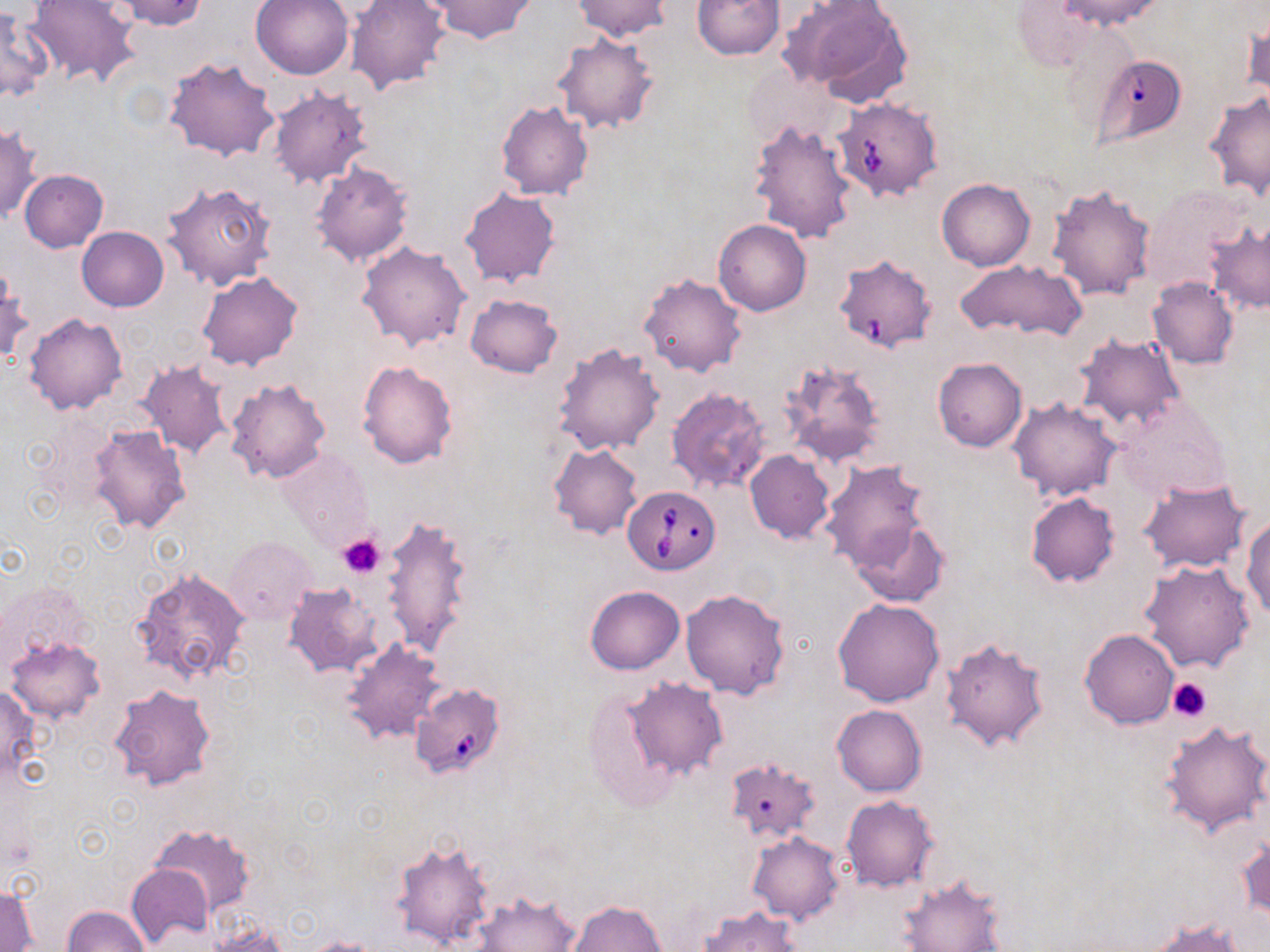
Summary:
  - Coordinate format: approximate bounding boxes as named x1/y1/x2/y2 corners in pixels
  - Platelet locations: (x1=338, y1=533, x2=385, y2=577), (x1=1166, y1=676, x2=1213, y2=723)
  - Uninfected red blood cell locations: (x1=25, y1=0, x2=140, y2=87), (x1=111, y1=0, x2=210, y2=30), (x1=250, y1=0, x2=355, y2=79), (x1=345, y1=0, x2=452, y2=97), (x1=427, y1=0, x2=536, y2=42), (x1=569, y1=0, x2=670, y2=41), (x1=692, y1=0, x2=784, y2=58), (x1=1049, y1=0, x2=1166, y2=33), (x1=783, y1=1, x2=913, y2=106), (x1=1006, y1=3, x2=1109, y2=72), (x1=0, y1=6, x2=51, y2=103), (x1=1244, y1=15, x2=1270, y2=106), (x1=553, y1=32, x2=659, y2=134), (x1=164, y1=56, x2=279, y2=162), (x1=1092, y1=58, x2=1186, y2=157), (x1=268, y1=86, x2=372, y2=190), (x1=1204, y1=91, x2=1270, y2=198), (x1=497, y1=100, x2=594, y2=200), (x1=832, y1=100, x2=940, y2=201), (x1=748, y1=118, x2=858, y2=244), (x1=0, y1=124, x2=40, y2=224), (x1=311, y1=163, x2=413, y2=267), (x1=20, y1=170, x2=108, y2=252), (x1=937, y1=178, x2=1035, y2=271), (x1=161, y1=180, x2=277, y2=290), (x1=1046, y1=183, x2=1156, y2=302), (x1=459, y1=187, x2=560, y2=288), (x1=714, y1=219, x2=811, y2=316), (x1=1206, y1=220, x2=1270, y2=315), (x1=77, y1=226, x2=169, y2=311), (x1=358, y1=241, x2=471, y2=352), (x1=838, y1=259, x2=938, y2=353), (x1=954, y1=259, x2=1085, y2=340), (x1=0, y1=267, x2=30, y2=366), (x1=197, y1=272, x2=303, y2=370), (x1=638, y1=272, x2=748, y2=377), (x1=1147, y1=277, x2=1239, y2=369), (x1=465, y1=294, x2=562, y2=378), (x1=23, y1=312, x2=127, y2=414), (x1=1074, y1=332, x2=1186, y2=432), (x1=553, y1=343, x2=664, y2=457), (x1=932, y1=357, x2=1026, y2=452), (x1=780, y1=359, x2=886, y2=468), (x1=357, y1=360, x2=458, y2=468), (x1=137, y1=362, x2=231, y2=458), (x1=226, y1=378, x2=332, y2=484), (x1=667, y1=386, x2=770, y2=495), (x1=1008, y1=398, x2=1122, y2=501), (x1=1114, y1=399, x2=1229, y2=501), (x1=89, y1=424, x2=191, y2=532), (x1=549, y1=443, x2=644, y2=540), (x1=277, y1=447, x2=371, y2=547), (x1=745, y1=450, x2=834, y2=544), (x1=821, y1=459, x2=935, y2=573), (x1=1138, y1=478, x2=1251, y2=573), (x1=1026, y1=492, x2=1119, y2=586), (x1=380, y1=516, x2=473, y2=657), (x1=850, y1=516, x2=949, y2=608), (x1=1244, y1=516, x2=1270, y2=620), (x1=226, y1=536, x2=317, y2=626), (x1=1137, y1=558, x2=1255, y2=673), (x1=134, y1=568, x2=250, y2=684), (x1=286, y1=582, x2=383, y2=677), (x1=585, y1=586, x2=684, y2=674), (x1=681, y1=588, x2=790, y2=698), (x1=833, y1=598, x2=944, y2=707), (x1=1079, y1=629, x2=1180, y2=729), (x1=5, y1=634, x2=105, y2=725), (x1=939, y1=638, x2=1049, y2=754), (x1=341, y1=639, x2=446, y2=744), (x1=623, y1=677, x2=729, y2=780), (x1=0, y1=685, x2=43, y2=780), (x1=108, y1=685, x2=217, y2=792), (x1=583, y1=687, x2=697, y2=809), (x1=832, y1=705, x2=926, y2=796), (x1=1160, y1=717, x2=1270, y2=838), (x1=724, y1=758, x2=821, y2=845), (x1=840, y1=796, x2=938, y2=891), (x1=149, y1=824, x2=255, y2=916), (x1=747, y1=832, x2=845, y2=923), (x1=1238, y1=833, x2=1269, y2=925), (x1=390, y1=839, x2=494, y2=951), (x1=126, y1=864, x2=212, y2=947), (x1=897, y1=875, x2=1005, y2=951), (x1=1, y1=885, x2=37, y2=951), (x1=471, y1=890, x2=580, y2=952), (x1=565, y1=900, x2=667, y2=952), (x1=62, y1=905, x2=149, y2=952), (x1=698, y1=905, x2=803, y2=952), (x1=1146, y1=919, x2=1248, y2=951), (x1=205, y1=920, x2=290, y2=951), (x1=302, y1=936, x2=386, y2=952)
  - Babesia divergens-infected red blood cell locations: (x1=624, y1=485, x2=718, y2=573), (x1=414, y1=686, x2=503, y2=779)
  - Slide-level diagnosis: Babesia divergens
  - Stain: May-Grünwald-Giemsa
  - Preparation: thin blood film
  - Image size: 1270×952 pixels
  - Modality: light microscopy
  - Field of view: one of a larger specimen
  - Magnification: 1000x